Classify this cell by malaria status.
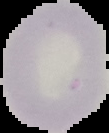

Uninfected.

Summary:
  - Preparation: thin blood smear
  - Image type: segmented cell region on a black background
  - Image size: 109×133 pixels